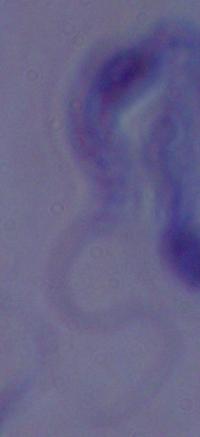

magnification: 1000x
identification: trypanosome
modality: micrograph